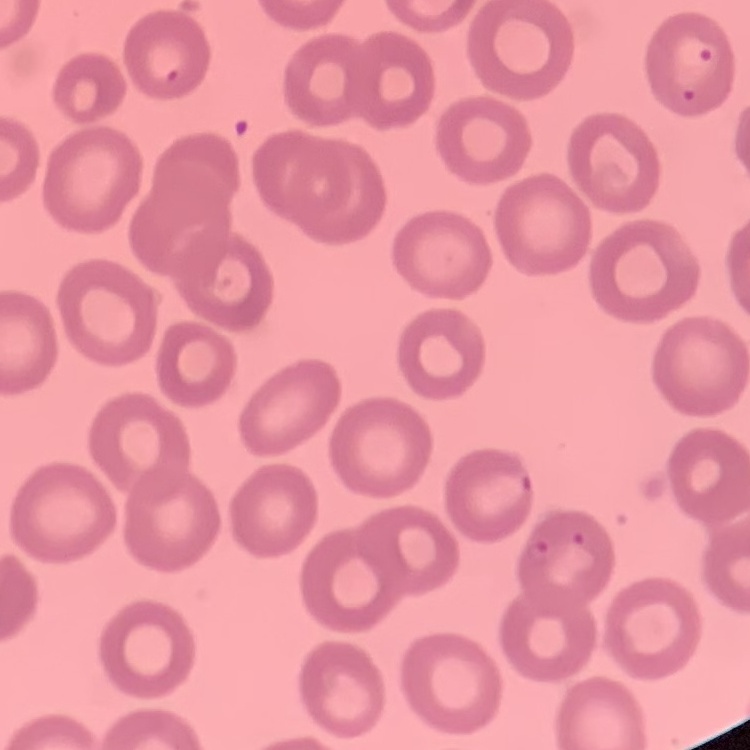
Summary:
  - Erythrocyte morphology: no rouleaux formation
  - Preparation: thin peripheral smear
  - Image type: one tile cut from a larger photomicrograph
  - Stain: Field's or Giemsa